Assess for parasitized red blood cells.
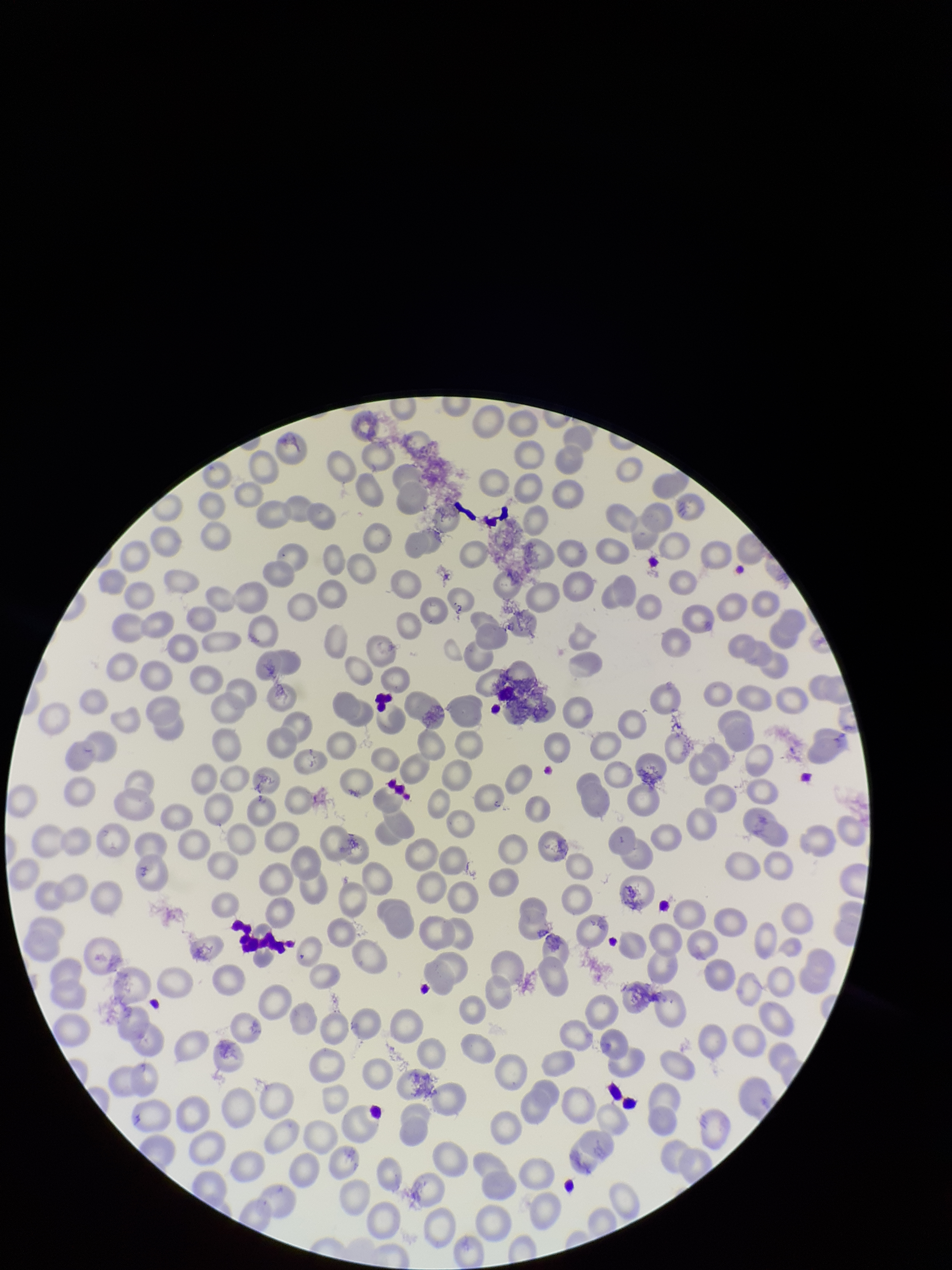
None seen.

{
  "red_blood_cell_count": 266,
  "preparation": "thin",
  "image_size": "952×1270 pixels",
  "stain": "Giemsa",
  "capture": "smartphone photograph through the microscope eyepiece",
  "patient_malaria_status": "negative",
  "parasitized_red_blood_cell_count": 0,
  "field_of_view": "single"
}